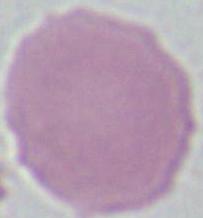 An erythrocyte is seen. Photomicrograph. Captured at 1000x magnification.